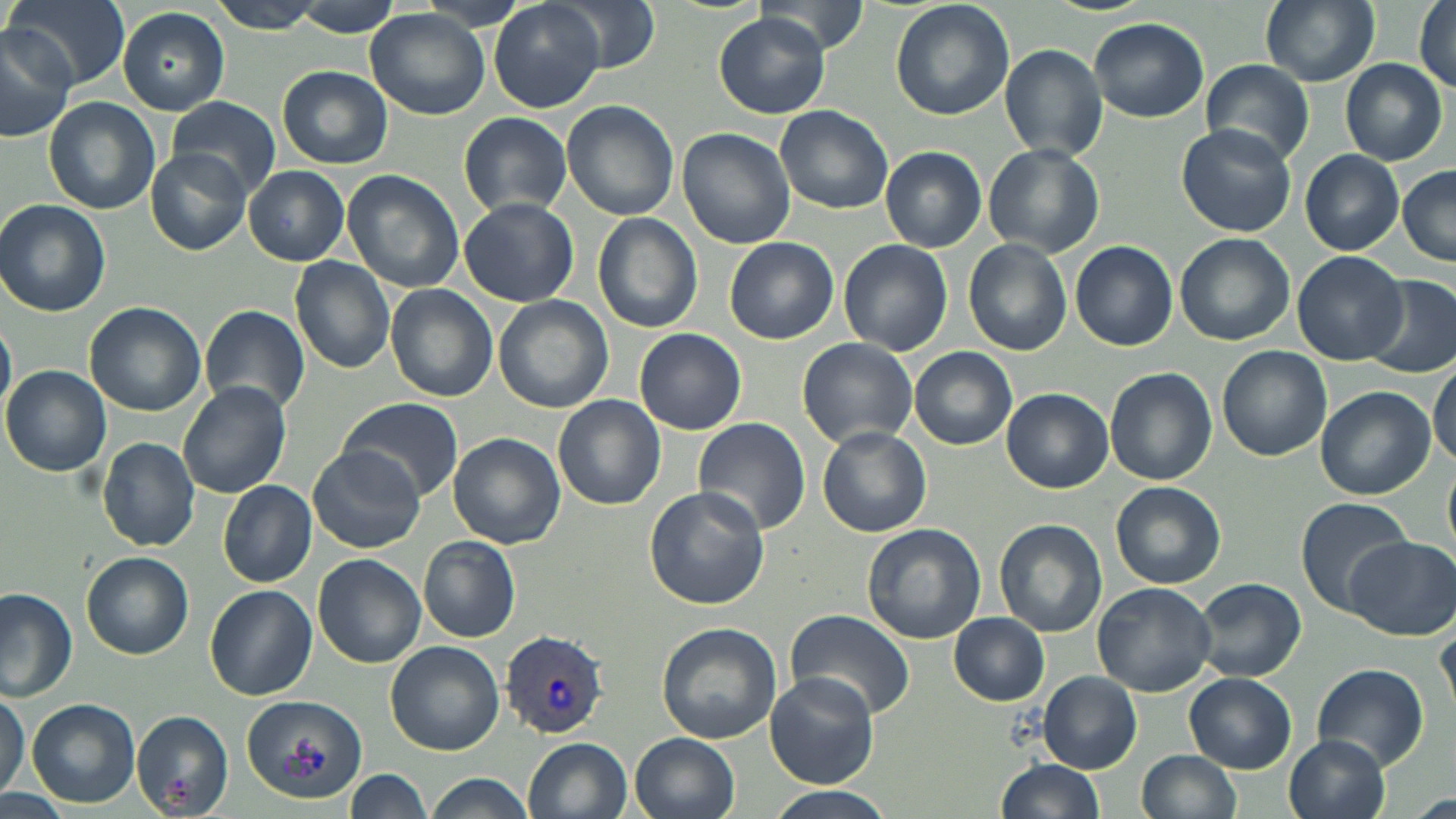 Approximate bounding boxes as named x1/y1/x2/y2 corners in pixels. Plasmodium vivax-infected red blood cell locations: (x1=500, y1=630, x2=608, y2=739). Uninfected red blood cell locations: (x1=4, y1=0, x2=129, y2=90), (x1=206, y1=0, x2=327, y2=34), (x1=414, y1=0, x2=533, y2=32), (x1=488, y1=0, x2=605, y2=112), (x1=548, y1=0, x2=659, y2=75), (x1=756, y1=0, x2=870, y2=53), (x1=890, y1=0, x2=1014, y2=120), (x1=1045, y1=0, x2=1154, y2=16), (x1=1259, y1=0, x2=1379, y2=87), (x1=1414, y1=0, x2=1456, y2=97), (x1=291, y1=3, x2=405, y2=38), (x1=116, y1=7, x2=230, y2=115), (x1=366, y1=11, x2=490, y2=119), (x1=715, y1=14, x2=831, y2=118), (x1=1089, y1=18, x2=1209, y2=122), (x1=0, y1=30, x2=72, y2=141), (x1=1000, y1=43, x2=1109, y2=163), (x1=1340, y1=58, x2=1447, y2=165), (x1=1201, y1=62, x2=1313, y2=160), (x1=276, y1=65, x2=392, y2=170), (x1=165, y1=95, x2=281, y2=196), (x1=43, y1=96, x2=161, y2=216), (x1=561, y1=100, x2=679, y2=220), (x1=775, y1=105, x2=894, y2=213), (x1=459, y1=112, x2=575, y2=217), (x1=1176, y1=124, x2=1297, y2=238), (x1=677, y1=125, x2=796, y2=248), (x1=985, y1=144, x2=1103, y2=256), (x1=881, y1=146, x2=987, y2=252), (x1=148, y1=147, x2=252, y2=254), (x1=1299, y1=150, x2=1404, y2=255), (x1=244, y1=166, x2=349, y2=266), (x1=1397, y1=166, x2=1456, y2=267), (x1=342, y1=170, x2=465, y2=291), (x1=459, y1=197, x2=579, y2=306), (x1=0, y1=200, x2=111, y2=316), (x1=592, y1=213, x2=703, y2=333), (x1=1175, y1=233, x2=1294, y2=346), (x1=724, y1=237, x2=839, y2=344), (x1=963, y1=237, x2=1072, y2=356), (x1=1069, y1=240, x2=1177, y2=351), (x1=840, y1=241, x2=953, y2=355), (x1=1293, y1=251, x2=1409, y2=366), (x1=290, y1=256, x2=396, y2=374), (x1=1361, y1=276, x2=1455, y2=376), (x1=385, y1=285, x2=499, y2=401), (x1=494, y1=295, x2=615, y2=414), (x1=85, y1=302, x2=206, y2=417), (x1=200, y1=304, x2=310, y2=418), (x1=0, y1=315, x2=16, y2=423), (x1=634, y1=328, x2=747, y2=435), (x1=796, y1=337, x2=918, y2=450), (x1=910, y1=345, x2=1017, y2=450), (x1=1217, y1=345, x2=1331, y2=461), (x1=1429, y1=361, x2=1455, y2=467), (x1=3, y1=365, x2=113, y2=476), (x1=1104, y1=367, x2=1217, y2=485), (x1=178, y1=380, x2=292, y2=499), (x1=1002, y1=387, x2=1114, y2=493), (x1=1315, y1=388, x2=1434, y2=500), (x1=554, y1=395, x2=666, y2=509), (x1=337, y1=398, x2=463, y2=506), (x1=693, y1=419, x2=812, y2=534), (x1=817, y1=427, x2=931, y2=537), (x1=448, y1=433, x2=566, y2=549), (x1=97, y1=438, x2=200, y2=551), (x1=309, y1=445, x2=425, y2=554), (x1=218, y1=479, x2=316, y2=586), (x1=1111, y1=481, x2=1226, y2=589), (x1=643, y1=485, x2=769, y2=610), (x1=1295, y1=496, x2=1410, y2=612), (x1=994, y1=519, x2=1107, y2=638), (x1=861, y1=521, x2=986, y2=645), (x1=419, y1=536, x2=520, y2=643), (x1=1345, y1=536, x2=1454, y2=640), (x1=82, y1=551, x2=193, y2=658), (x1=314, y1=554, x2=425, y2=669), (x1=1194, y1=579, x2=1307, y2=681), (x1=1092, y1=581, x2=1217, y2=695), (x1=205, y1=583, x2=316, y2=700), (x1=0, y1=589, x2=77, y2=701), (x1=785, y1=610, x2=915, y2=719), (x1=949, y1=614, x2=1049, y2=705), (x1=1434, y1=618, x2=1456, y2=718), (x1=655, y1=623, x2=782, y2=744), (x1=384, y1=640, x2=504, y2=756), (x1=1313, y1=663, x2=1429, y2=770), (x1=764, y1=671, x2=881, y2=787), (x1=1038, y1=672, x2=1141, y2=773), (x1=1185, y1=674, x2=1296, y2=774), (x1=0, y1=689, x2=27, y2=801), (x1=241, y1=694, x2=367, y2=801), (x1=27, y1=698, x2=140, y2=808), (x1=132, y1=710, x2=237, y2=819), (x1=630, y1=733, x2=741, y2=819), (x1=1285, y1=734, x2=1392, y2=819), (x1=524, y1=736, x2=634, y2=819), (x1=1137, y1=750, x2=1242, y2=819), (x1=995, y1=759, x2=1105, y2=818), (x1=345, y1=768, x2=434, y2=818), (x1=426, y1=772, x2=534, y2=819), (x1=0, y1=787, x2=73, y2=818), (x1=765, y1=787, x2=891, y2=819), (x1=1408, y1=791, x2=1455, y2=819). Slide-level diagnosis: Plasmodium vivax. Optical microscopy. Captured at 1000x magnification. Image is 1456×819 pixels. May-Grünwald-Giemsa-stained preparation. One field of a larger specimen. Thin blood film.